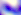
Photomicrograph. Captured at 400x magnification. Toxoplasma gondii is shown.